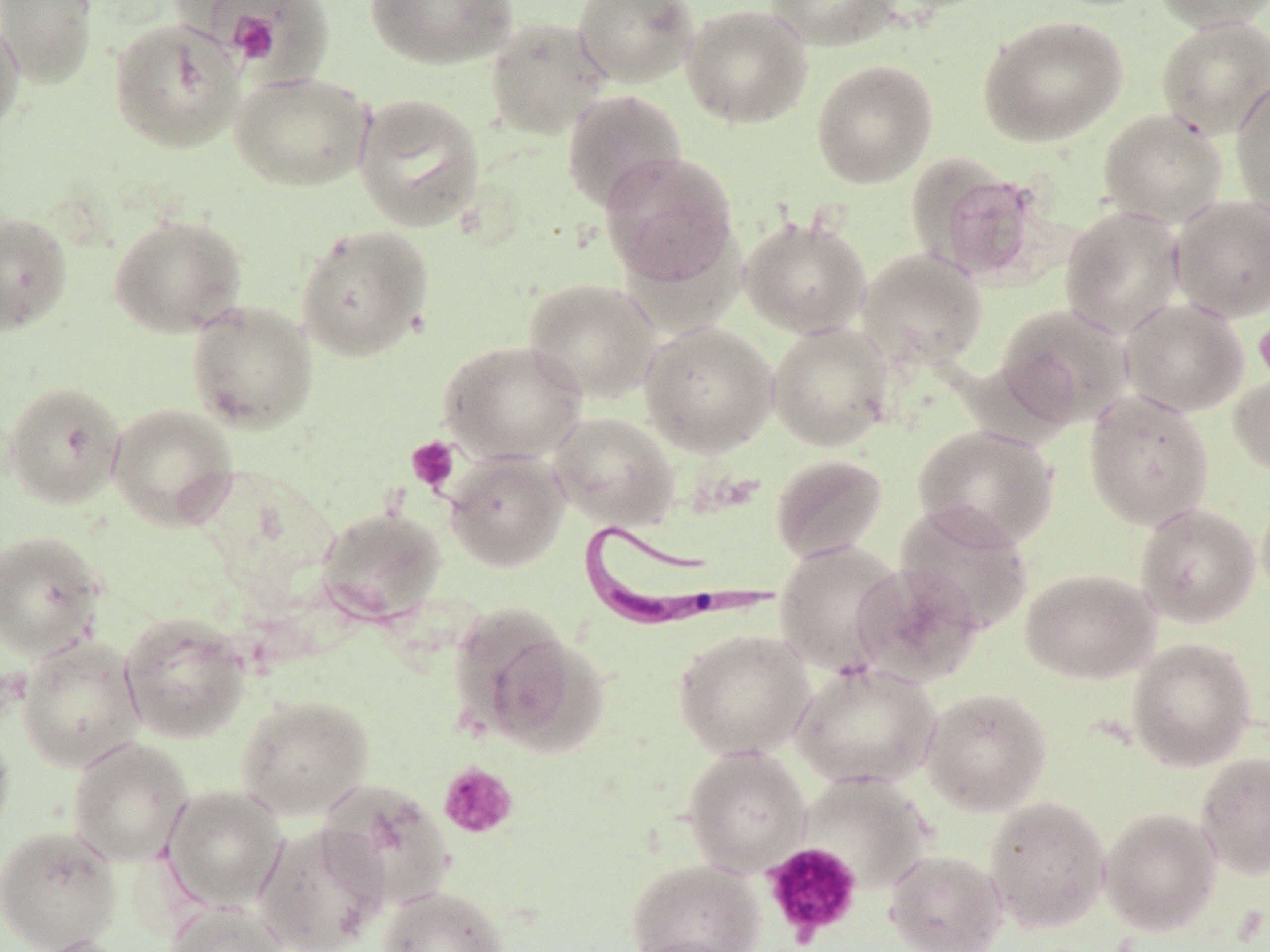

Approximate bounding boxes as (x1, y1, x2, y2) in pixels. Uninfected red blood cell locations: (0, 0, 98, 89), (364, 0, 519, 69), (572, 0, 700, 88), (765, 0, 899, 50), (1151, 0, 1270, 31), (681, 4, 812, 128), (0, 15, 26, 136), (978, 15, 1128, 146), (1156, 15, 1270, 139), (109, 17, 245, 154), (485, 17, 610, 139), (811, 58, 938, 188), (230, 70, 374, 191), (1231, 77, 1270, 221), (561, 89, 687, 213), (353, 93, 486, 232), (1098, 108, 1228, 229), (598, 151, 739, 288), (920, 163, 1050, 285), (1169, 194, 1270, 323), (1059, 205, 1186, 339), (0, 212, 73, 334), (108, 213, 249, 338), (740, 215, 872, 339), (294, 224, 434, 362), (857, 248, 988, 369), (522, 277, 661, 403), (1120, 297, 1249, 417), (186, 299, 318, 433), (994, 303, 1134, 430), (639, 320, 778, 457), (767, 321, 895, 451), (438, 339, 587, 464), (1228, 369, 1270, 478), (3, 381, 126, 508), (1084, 390, 1215, 530), (107, 403, 239, 530), (548, 411, 680, 531), (912, 425, 1060, 551), (443, 450, 570, 573), (770, 454, 889, 563), (1256, 486, 1270, 606), (893, 501, 1034, 637), (1134, 502, 1261, 629), (315, 505, 448, 624), (0, 530, 108, 662), (774, 541, 908, 678), (851, 561, 986, 687), (1019, 567, 1160, 684), (451, 605, 588, 748), (119, 611, 253, 744), (673, 628, 815, 759), (16, 636, 146, 772), (1125, 637, 1257, 771), (790, 661, 940, 790), (921, 687, 1052, 816), (235, 693, 374, 820), (0, 718, 15, 850), (67, 737, 193, 867), (681, 745, 812, 876), (1194, 751, 1270, 880), (799, 772, 934, 893), (316, 779, 456, 911), (162, 785, 287, 912), (984, 795, 1111, 933), (1099, 807, 1222, 935), (252, 823, 388, 952), (0, 824, 122, 952), (885, 848, 1008, 952), (624, 858, 765, 952), (379, 885, 509, 952), (164, 902, 290, 952), (31, 935, 138, 952). Platelet locations: (219, 4, 294, 68), (1253, 316, 1270, 385), (406, 436, 460, 492), (438, 761, 519, 839), (761, 841, 863, 945). Trypanosoma brucei locations: (576, 518, 786, 634). Slide-level diagnosis: Trypanosoma brucei. Single field of view. Thin blood film. May-Grünwald-Giemsa stain. Optical microscopy. Captured at 1000x magnification. Image is 1270×952 pixels.